Locate every Plasmodium parasite.
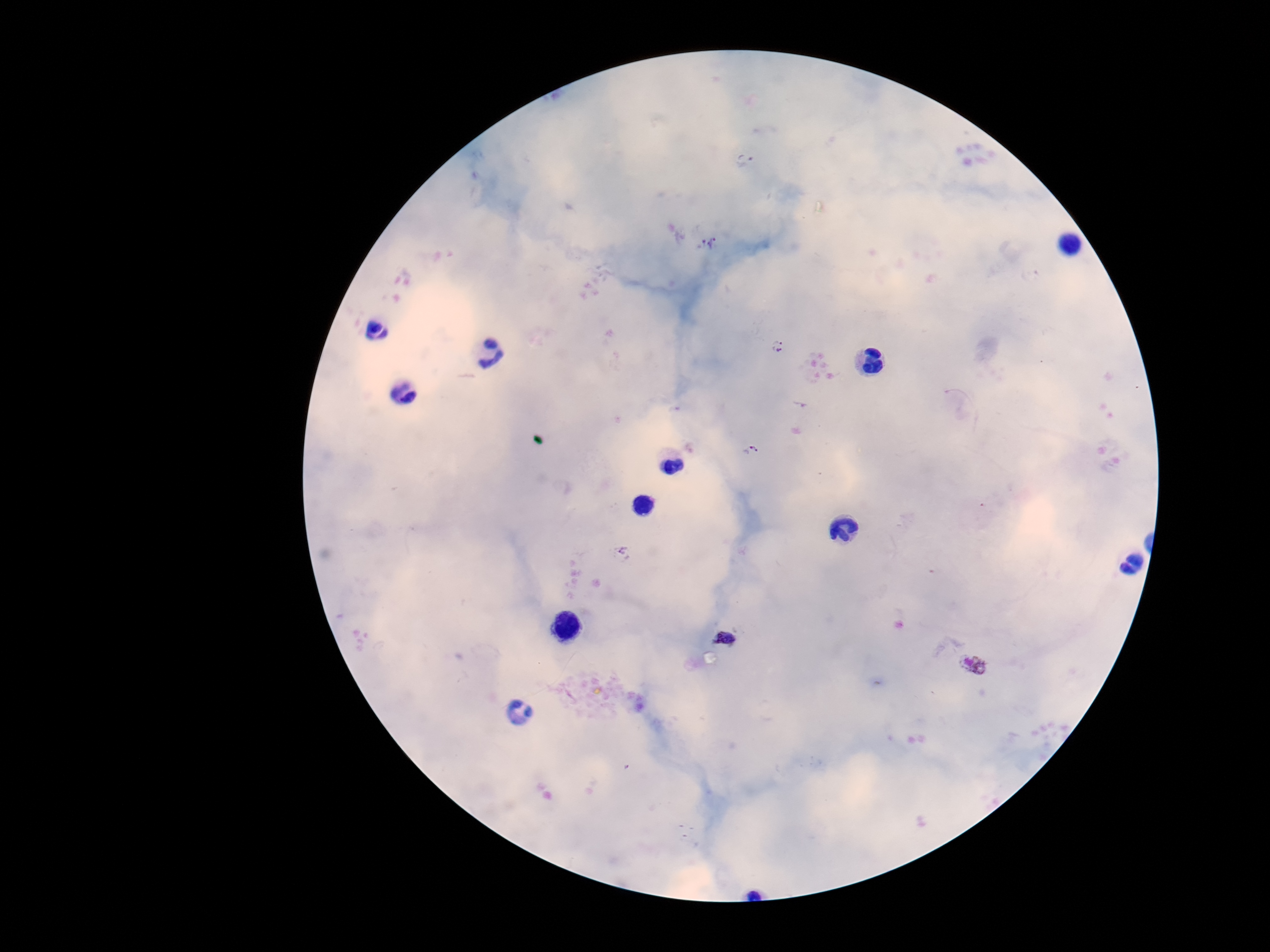

Approximate centers as (x, y) in pixels.
Plasmodium parasites: (745, 160), (695, 242), (718, 244), (778, 339), (776, 355), (801, 404), (752, 450), (621, 552), (726, 638), (975, 664).

Smartphone photograph taken through the microscope eyepiece. Patient malaria status: infected. Thick blood smear. Image is 1270×952 pixels. 100x magnification. One field from this slide. Giemsa-stained preparation.